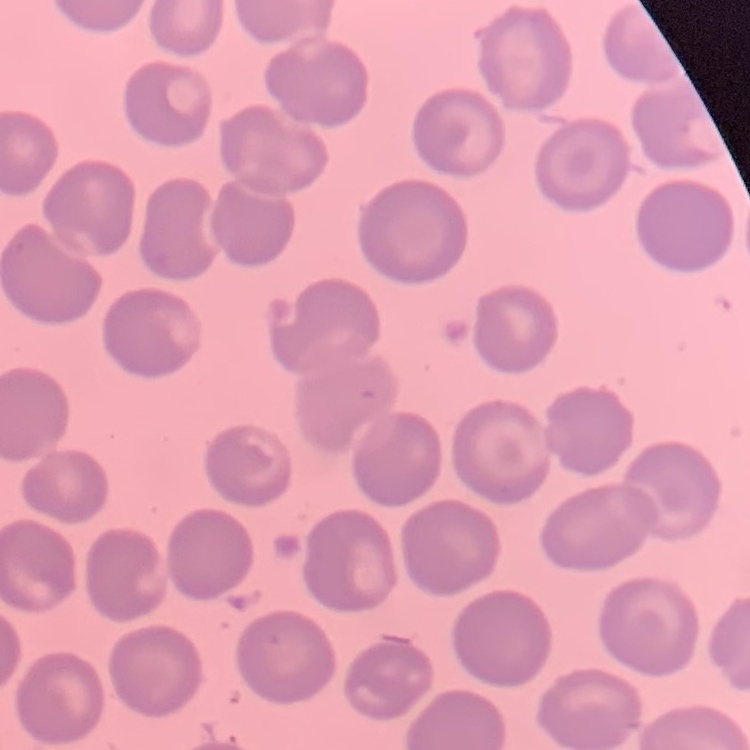
Summary:
  - Erythrocyte morphology: no rouleaux formation
  - Image type: square crop of a larger photomicrograph
  - Preparation: thin blood smear
  - Stain: Field's or Giemsa